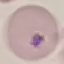
malaria status = uninfected
stain = Giemsa
image type = cell patch, automatically extracted from a larger field of view and resized to 64 × 64 pixels
capture = smartphone camera at the microscope eyepiece
preparation = thin blood smear